Locate every blood parasite and identify its species.
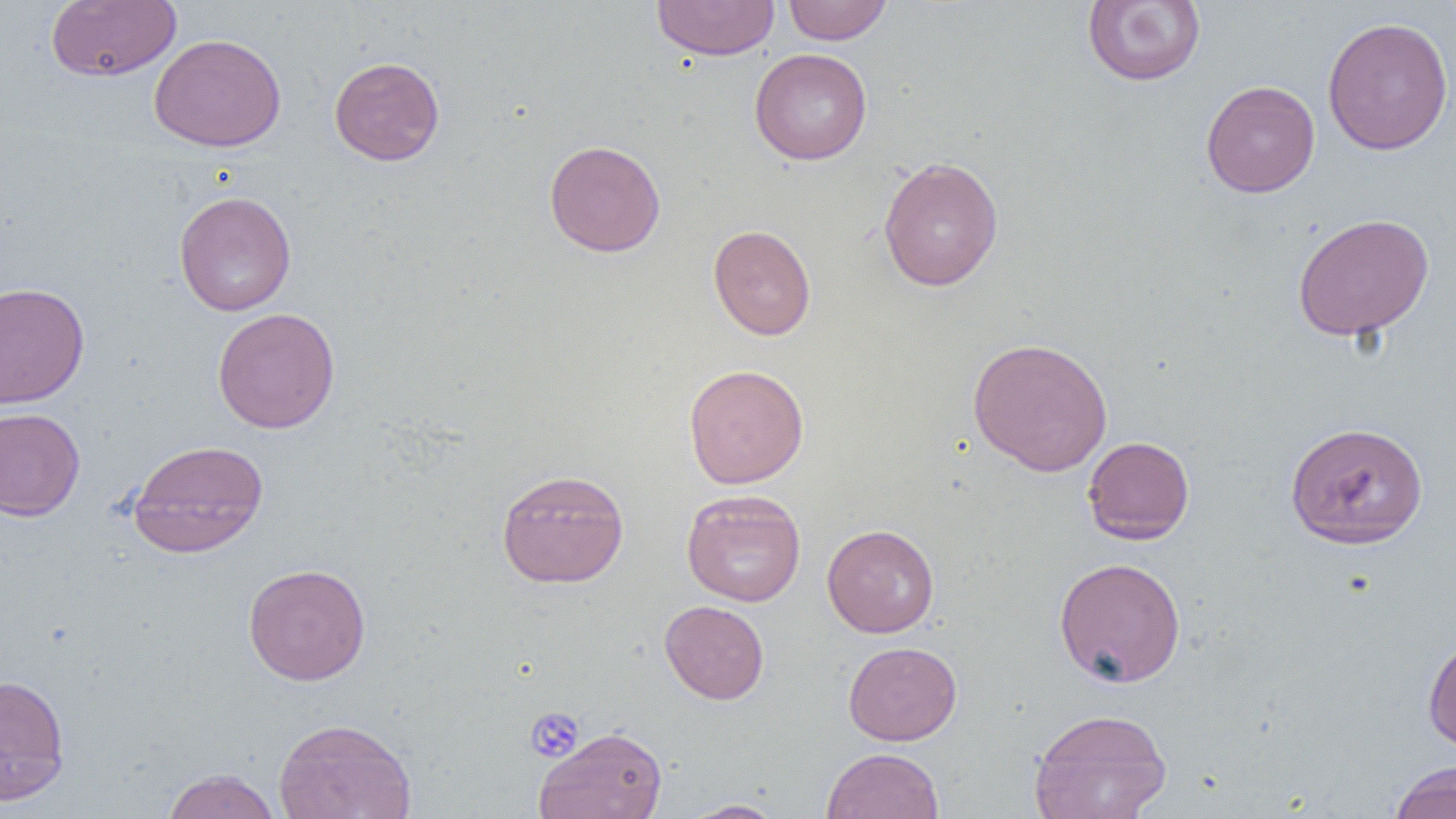
No blood parasites seen.

slide-level diagnosis = negative for blood parasites
magnification = 1000x
preparation = thin blood film
modality = light microscopy
field of view = one of a larger specimen
uninfected red blood cell locations = approximate bounding boxes as (x1,y1)-(x2,y2) corner pairs in pixels: (651,0)-(781,61), (783,0)-(892,45), (1082,0)-(1206,87), (46,1)-(181,82), (1322,16)-(1453,155), (148,33)-(286,152), (749,48)-(873,165), (329,56)-(445,166), (1201,80)-(1319,198), (543,139)-(666,257), (878,156)-(1004,291), (174,190)-(297,316), (1293,213)-(1434,341), (708,224)-(816,340), (0,282)-(89,408), (212,307)-(341,434), (968,337)-(1113,476), (683,364)-(809,489), (0,408)-(85,521), (1285,421)-(1429,549), (1082,436)-(1195,544), (127,439)-(269,558), (496,469)-(629,588), (681,489)-(806,606), (822,523)-(940,637), (1054,556)-(1186,688), (243,563)-(371,686), (659,600)-(769,704), (1422,633)-(1456,754), (843,641)-(962,745), (0,673)-(71,805), (1028,708)-(1172,819), (273,717)-(417,819), (534,726)-(667,819), (821,747)-(944,819), (1388,761)-(1456,819), (161,768)-(281,819), (681,799)-(787,818)
image size = 1456×819 pixels
platelet locations = approximate bounding boxes as (x1,y1)-(x2,y2) corner pairs in pixels: (525,707)-(585,763)